Point out every Plasmodium parasite and every leukocyte.
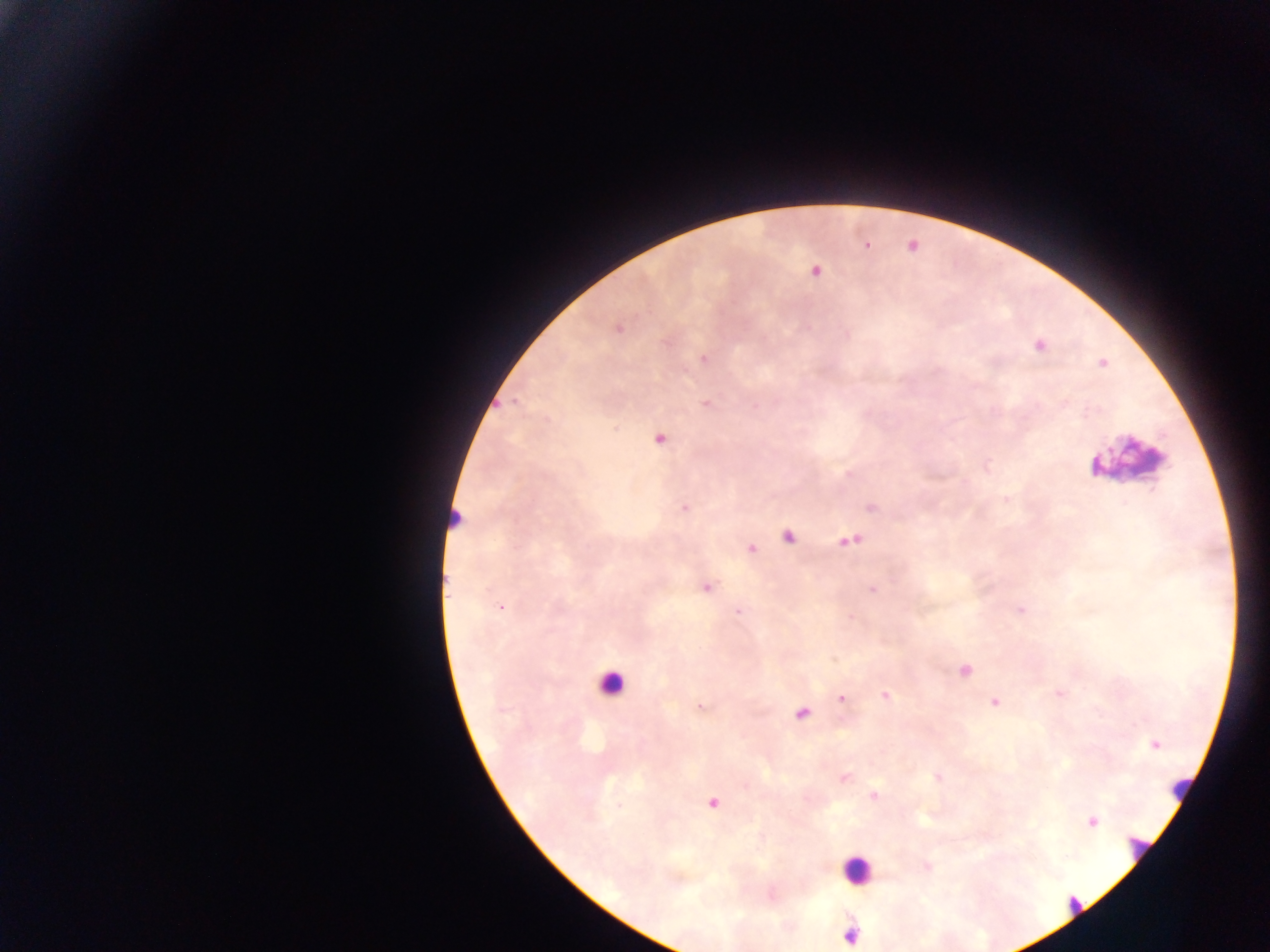
Approximate centers as [x, y] in pixels.
Plasmodium parasites: [867, 246], [815, 270], [1038, 344], [703, 358], [1102, 362], [1062, 402], [704, 403], [1086, 413], [613, 426], [658, 437], [1094, 465], [987, 467], [1006, 499], [870, 507], [683, 509], [456, 519], [787, 535], [848, 542], [750, 548], [706, 588], [872, 590], [1020, 609], [739, 612], [833, 659], [965, 671], [886, 694], [841, 700], [993, 703], [700, 706], [802, 712], [1154, 744], [937, 777], [845, 779], [874, 795], [712, 803], [619, 806], [1091, 821], [927, 868], [849, 934].
Leukocytes (some below the resolvable threshold): [1136, 466], [612, 682], [1178, 787], [1135, 850], [857, 874], [1068, 907].

Collected in Ghana. Image is 1270×952 pixels. Thick blood smear. Single field of view. Photographed through a microscope with a mobile-phone camera.